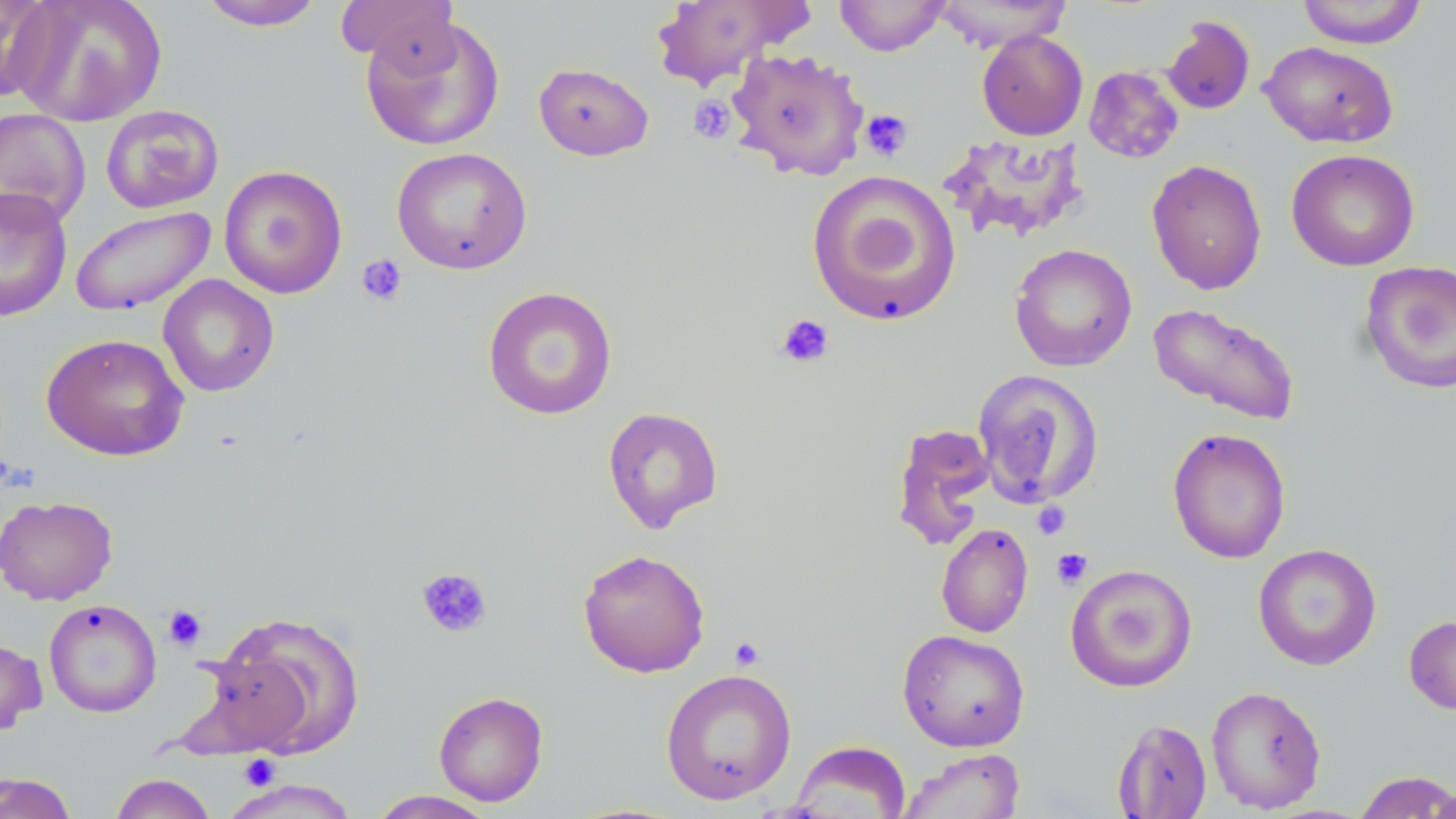
Approximate bounding boxes as [x1, y1, x2, y2] in pixels. Uninfected red blood cell locations: [0, 0, 55, 103], [11, 0, 167, 126], [195, 0, 326, 31], [334, 0, 459, 73], [649, 0, 811, 89], [834, 0, 949, 56], [931, 0, 1073, 52], [1295, 0, 1429, 48], [360, 15, 506, 152], [1162, 15, 1256, 115], [977, 29, 1088, 141], [1260, 41, 1399, 148], [726, 48, 870, 181], [533, 62, 654, 160], [1084, 66, 1184, 164], [100, 104, 224, 214], [0, 107, 91, 228], [938, 132, 1089, 244], [392, 146, 532, 274], [1286, 149, 1420, 272], [1146, 159, 1268, 295], [218, 165, 348, 299], [806, 170, 962, 328], [0, 186, 73, 322], [69, 205, 216, 316], [1009, 243, 1138, 371], [1358, 259, 1456, 395], [158, 274, 279, 397], [482, 286, 618, 420], [1148, 301, 1302, 426], [40, 332, 190, 461], [972, 369, 1104, 509], [602, 406, 724, 534], [890, 422, 997, 552], [1167, 427, 1291, 564], [0, 495, 118, 606], [936, 523, 1034, 637], [1253, 543, 1382, 671], [578, 548, 710, 678], [1065, 564, 1198, 692], [43, 598, 162, 718], [209, 611, 365, 759], [1404, 614, 1456, 716], [897, 629, 1030, 752], [0, 634, 47, 737], [661, 667, 797, 805], [1205, 685, 1327, 814], [433, 690, 549, 806], [1112, 719, 1212, 818], [790, 740, 911, 819], [898, 748, 1024, 819], [1353, 770, 1456, 818], [0, 772, 78, 818], [108, 773, 217, 819], [219, 778, 362, 819], [1425, 782, 1456, 819], [368, 790, 499, 819]. Platelet locations: [688, 95, 736, 144], [859, 109, 912, 162], [356, 254, 408, 306], [775, 313, 835, 368], [1032, 501, 1072, 540], [1052, 548, 1093, 589], [416, 567, 493, 639], [162, 604, 207, 652], [729, 636, 765, 670], [238, 754, 281, 791]. Slide-level diagnosis: no evidence of blood parasites. Thin blood film. May-Grünwald-Giemsa stain. One field of a larger specimen. 1000x magnification. Optical microscopy. Image is 1456×819 pixels.